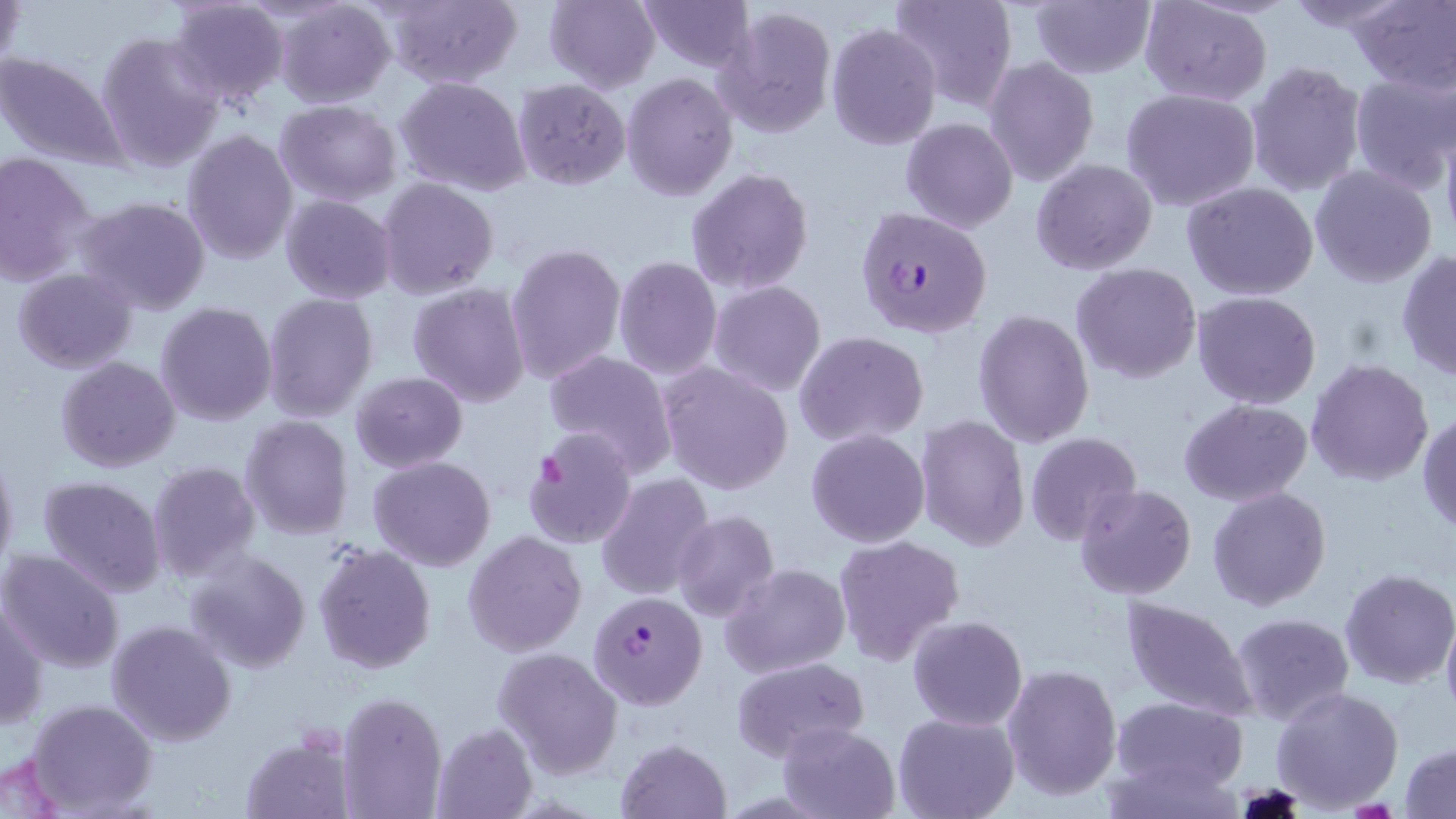 Approximate bounding boxes as named x1/y1/x2/y2 corners in pixels. Plasmodium falciparum-infected red blood cell locations: (x1=854, y1=206, x2=993, y2=340), (x1=586, y1=591, x2=706, y2=711). Uninfected red blood cell locations: (x1=1, y1=0, x2=26, y2=81), (x1=165, y1=0, x2=290, y2=110), (x1=275, y1=0, x2=395, y2=108), (x1=379, y1=0, x2=521, y2=88), (x1=542, y1=0, x2=660, y2=92), (x1=638, y1=0, x2=756, y2=72), (x1=887, y1=0, x2=1016, y2=115), (x1=1027, y1=0, x2=1156, y2=79), (x1=1139, y1=0, x2=1273, y2=107), (x1=1282, y1=0, x2=1411, y2=34), (x1=1348, y1=1, x2=1456, y2=92), (x1=714, y1=4, x2=837, y2=138), (x1=826, y1=23, x2=941, y2=149), (x1=94, y1=30, x2=224, y2=173), (x1=0, y1=50, x2=131, y2=172), (x1=985, y1=57, x2=1098, y2=186), (x1=1245, y1=60, x2=1366, y2=198), (x1=1348, y1=70, x2=1455, y2=192), (x1=623, y1=73, x2=738, y2=201), (x1=395, y1=75, x2=532, y2=196), (x1=512, y1=79, x2=632, y2=190), (x1=1121, y1=87, x2=1260, y2=211), (x1=273, y1=98, x2=402, y2=204), (x1=899, y1=117, x2=1018, y2=234), (x1=1442, y1=128, x2=1456, y2=247), (x1=182, y1=129, x2=299, y2=265), (x1=0, y1=151, x2=97, y2=284), (x1=1031, y1=157, x2=1157, y2=275), (x1=1309, y1=164, x2=1438, y2=288), (x1=686, y1=168, x2=814, y2=294), (x1=376, y1=177, x2=499, y2=300), (x1=1182, y1=181, x2=1319, y2=300), (x1=280, y1=194, x2=398, y2=305), (x1=74, y1=197, x2=212, y2=317), (x1=506, y1=242, x2=627, y2=384), (x1=1396, y1=248, x2=1456, y2=383), (x1=612, y1=255, x2=722, y2=378), (x1=1070, y1=263, x2=1202, y2=385), (x1=11, y1=267, x2=138, y2=374), (x1=708, y1=280, x2=827, y2=396), (x1=407, y1=281, x2=530, y2=409), (x1=1192, y1=290, x2=1322, y2=409), (x1=263, y1=294, x2=379, y2=423), (x1=154, y1=300, x2=276, y2=427), (x1=972, y1=309, x2=1094, y2=448), (x1=794, y1=330, x2=929, y2=447), (x1=542, y1=349, x2=678, y2=474), (x1=55, y1=356, x2=181, y2=474), (x1=1306, y1=358, x2=1435, y2=487), (x1=658, y1=363, x2=795, y2=495), (x1=350, y1=371, x2=468, y2=473), (x1=1179, y1=398, x2=1313, y2=507), (x1=1418, y1=409, x2=1456, y2=535), (x1=916, y1=415, x2=1030, y2=553), (x1=240, y1=416, x2=354, y2=539), (x1=520, y1=427, x2=637, y2=549), (x1=806, y1=428, x2=930, y2=548), (x1=1024, y1=432, x2=1143, y2=545), (x1=0, y1=447, x2=19, y2=578), (x1=369, y1=455, x2=495, y2=572), (x1=147, y1=461, x2=260, y2=581), (x1=594, y1=472, x2=717, y2=601), (x1=37, y1=476, x2=167, y2=598), (x1=1075, y1=484, x2=1198, y2=600), (x1=1207, y1=485, x2=1331, y2=611), (x1=670, y1=510, x2=780, y2=624), (x1=463, y1=530, x2=587, y2=656), (x1=832, y1=533, x2=966, y2=666), (x1=313, y1=543, x2=437, y2=674), (x1=0, y1=549, x2=125, y2=673), (x1=184, y1=550, x2=312, y2=673), (x1=720, y1=562, x2=850, y2=678), (x1=1339, y1=568, x2=1455, y2=688), (x1=1118, y1=595, x2=1259, y2=721), (x1=0, y1=597, x2=48, y2=733), (x1=1441, y1=609, x2=1456, y2=725), (x1=1232, y1=612, x2=1355, y2=727), (x1=907, y1=614, x2=1029, y2=731), (x1=106, y1=619, x2=237, y2=748), (x1=1248, y1=629, x2=1385, y2=783), (x1=491, y1=647, x2=624, y2=779), (x1=731, y1=657, x2=870, y2=763), (x1=1002, y1=663, x2=1123, y2=801), (x1=1271, y1=685, x2=1403, y2=811), (x1=337, y1=691, x2=446, y2=819), (x1=1111, y1=696, x2=1246, y2=797), (x1=26, y1=698, x2=157, y2=816), (x1=892, y1=710, x2=1019, y2=819), (x1=777, y1=721, x2=900, y2=819), (x1=432, y1=722, x2=539, y2=818), (x1=239, y1=731, x2=354, y2=819), (x1=615, y1=738, x2=732, y2=819), (x1=1401, y1=742, x2=1456, y2=818), (x1=0, y1=752, x2=69, y2=819). Slide-level diagnosis: Plasmodium falciparum. Thin blood film. Image is 1456×819 pixels. Captured at 1000x magnification. Single field of view. May-Grünwald-Giemsa stain. Optical microscopy.